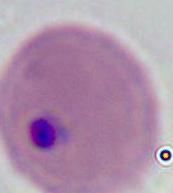
modality = photomicrograph
identification = Plasmodium
magnification = 400x or 1000x